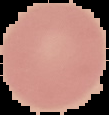

From a thin blood film. Image is 109×115 pixels. Malaria status: uninfected. The area outside the segmented cell region is set to black.